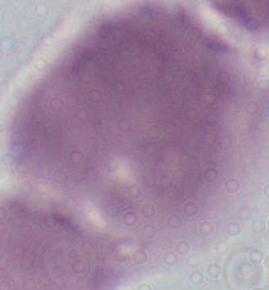

A red blood cell is seen. Micrograph. 1000x magnification.